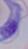
identification = trypanosome
modality = micrograph
magnification = 1000x